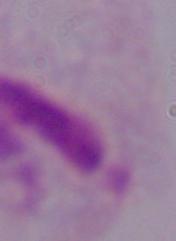
{
  "magnification": "1000x",
  "modality": "photomicrograph",
  "identification": "trichomonad"
}